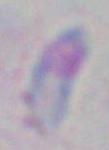

Captured at 1000x magnification. Micrograph. Toxoplasma gondii is seen.